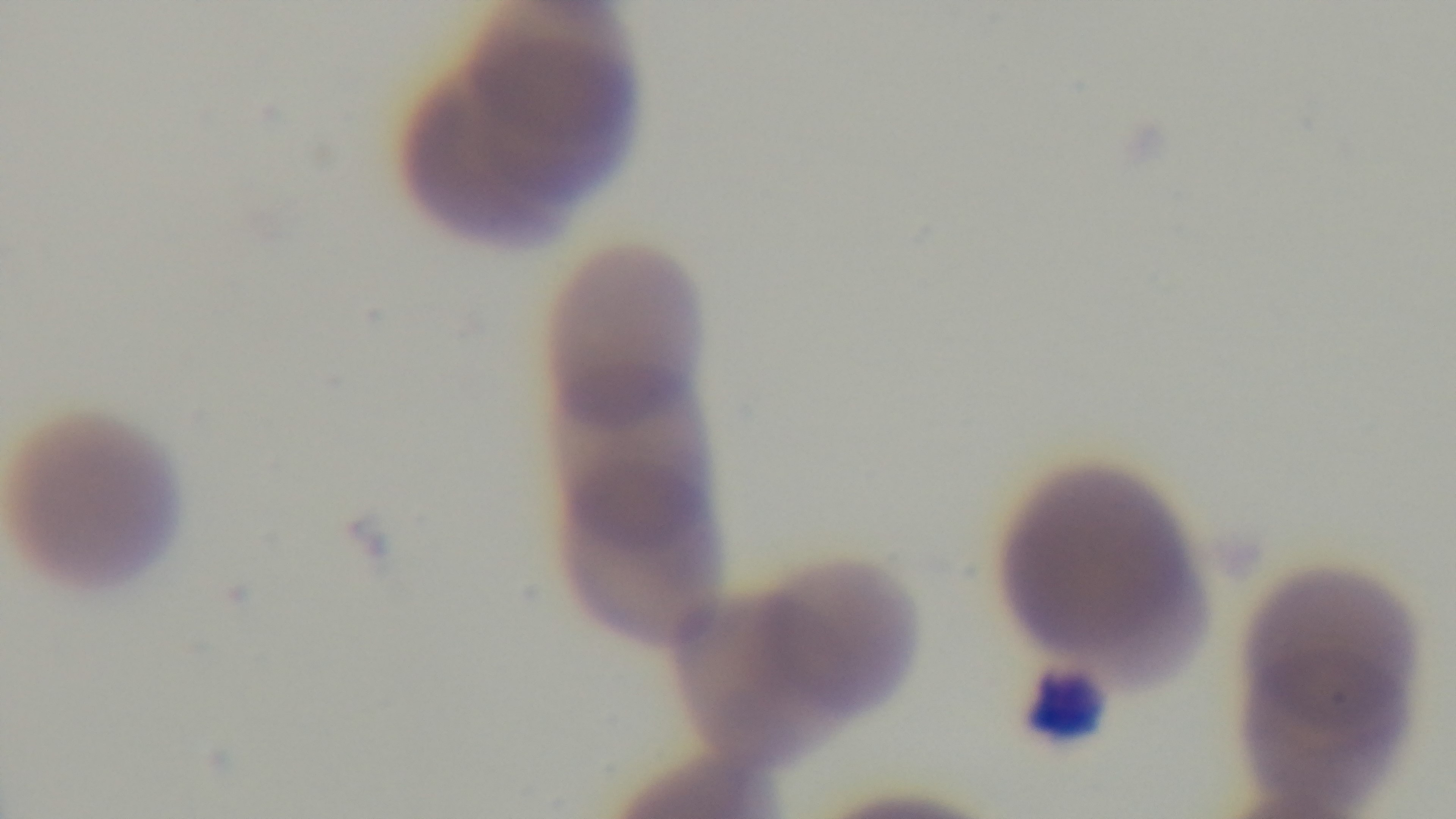

Giemsa-stained. 100x oil-immersion objective. One field from the slide. Mounted 4K digital camera. Malaria status: positive. Light microscopy. Preparation: thin blood film.